Outline each blood parasite and name the species.
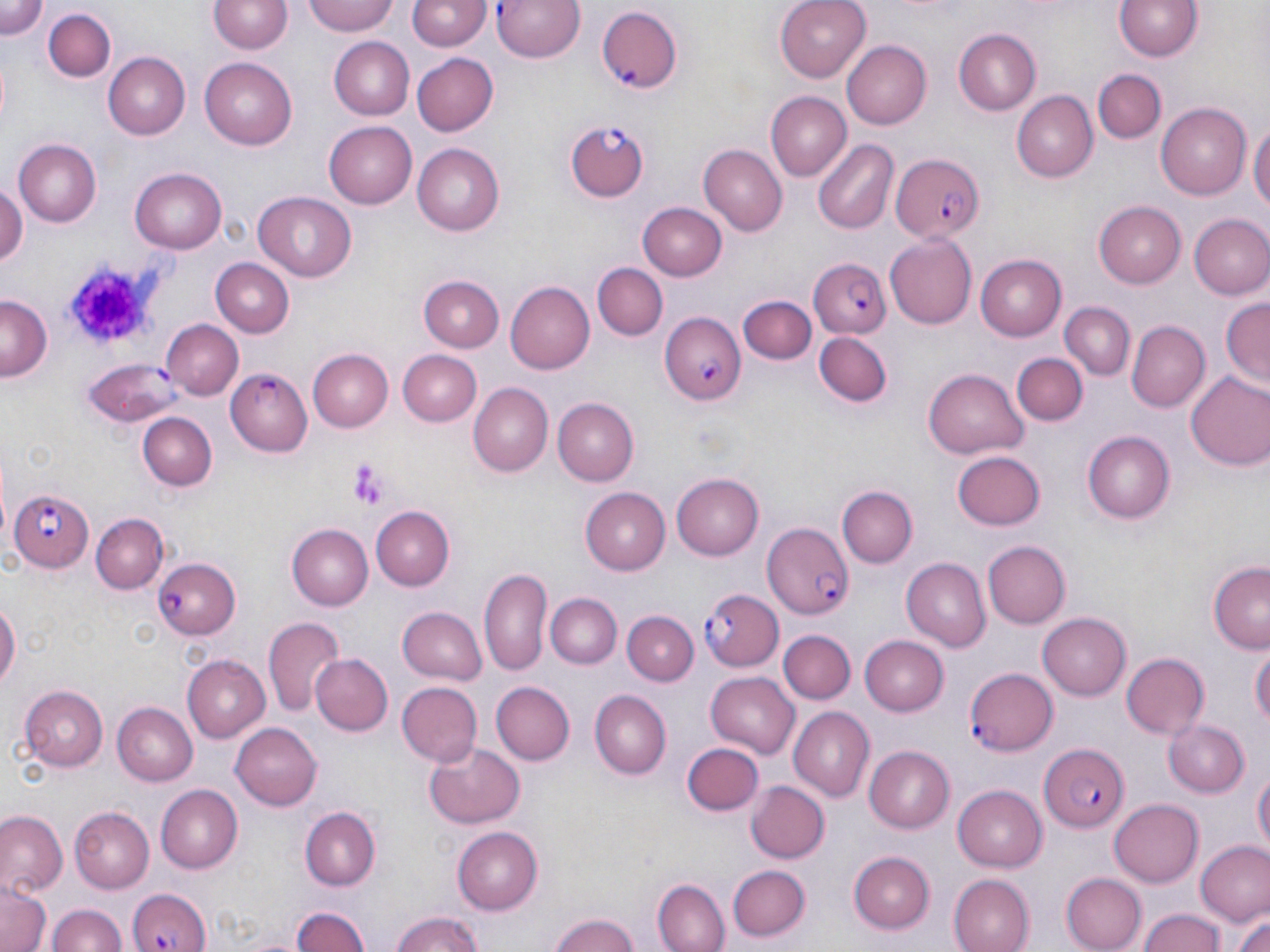

Approximate bounding boxes as named x1/y1/x2/y2 corners in pixels.
Plasmodium falciparum-infected red blood cells: (x1=494, y1=0, x2=587, y2=65), (x1=596, y1=6, x2=684, y2=91), (x1=566, y1=122, x2=650, y2=199), (x1=892, y1=154, x2=985, y2=243), (x1=807, y1=257, x2=892, y2=339), (x1=660, y1=311, x2=744, y2=406), (x1=83, y1=360, x2=183, y2=425), (x1=224, y1=369, x2=313, y2=457), (x1=11, y1=489, x2=92, y2=573), (x1=760, y1=522, x2=853, y2=618), (x1=155, y1=557, x2=240, y2=639), (x1=700, y1=589, x2=782, y2=670), (x1=964, y1=666, x2=1057, y2=756), (x1=1037, y1=742, x2=1130, y2=832), (x1=127, y1=886, x2=210, y2=952).
No Plasmodium ovale, Plasmodium malariae, Plasmodium vivax, Babesia divergens, or Trypanosoma brucei observed.

Platelet locations: (x1=65, y1=258, x2=160, y2=350), (x1=348, y1=461, x2=390, y2=510). Uninfected red blood cell locations: (x1=0, y1=0, x2=49, y2=39), (x1=302, y1=0, x2=399, y2=37), (x1=773, y1=0, x2=871, y2=83), (x1=1113, y1=0, x2=1206, y2=62), (x1=209, y1=1, x2=291, y2=55), (x1=408, y1=1, x2=488, y2=51), (x1=42, y1=7, x2=116, y2=80), (x1=951, y1=28, x2=1041, y2=115), (x1=328, y1=36, x2=414, y2=118), (x1=840, y1=38, x2=930, y2=130), (x1=410, y1=52, x2=496, y2=137), (x1=104, y1=53, x2=190, y2=138), (x1=200, y1=58, x2=297, y2=147), (x1=1094, y1=70, x2=1164, y2=143), (x1=1010, y1=90, x2=1098, y2=181), (x1=764, y1=91, x2=850, y2=180), (x1=1156, y1=104, x2=1252, y2=198), (x1=1250, y1=119, x2=1269, y2=224), (x1=325, y1=123, x2=416, y2=207), (x1=813, y1=139, x2=898, y2=234), (x1=13, y1=140, x2=102, y2=227), (x1=412, y1=144, x2=505, y2=235), (x1=698, y1=146, x2=787, y2=234), (x1=131, y1=168, x2=227, y2=253), (x1=0, y1=183, x2=25, y2=273), (x1=254, y1=193, x2=357, y2=281), (x1=1093, y1=201, x2=1187, y2=287), (x1=639, y1=203, x2=726, y2=280), (x1=1189, y1=214, x2=1270, y2=299), (x1=885, y1=234, x2=976, y2=329), (x1=975, y1=255, x2=1066, y2=340), (x1=210, y1=258, x2=293, y2=336), (x1=592, y1=263, x2=667, y2=341), (x1=420, y1=273, x2=504, y2=352), (x1=503, y1=281, x2=594, y2=375), (x1=0, y1=296, x2=50, y2=380), (x1=738, y1=296, x2=815, y2=364), (x1=1221, y1=299, x2=1269, y2=391), (x1=1061, y1=302, x2=1133, y2=380), (x1=1126, y1=319, x2=1209, y2=411), (x1=160, y1=320, x2=241, y2=401), (x1=816, y1=330, x2=894, y2=408), (x1=309, y1=350, x2=395, y2=433), (x1=397, y1=351, x2=481, y2=425), (x1=1014, y1=354, x2=1085, y2=426), (x1=923, y1=369, x2=1029, y2=459), (x1=1185, y1=371, x2=1270, y2=472), (x1=470, y1=383, x2=552, y2=476), (x1=551, y1=398, x2=638, y2=486), (x1=139, y1=412, x2=215, y2=490), (x1=1083, y1=432, x2=1176, y2=524), (x1=952, y1=451, x2=1045, y2=530), (x1=672, y1=474, x2=765, y2=559), (x1=839, y1=486, x2=918, y2=568), (x1=580, y1=488, x2=670, y2=573), (x1=369, y1=506, x2=453, y2=590), (x1=91, y1=512, x2=167, y2=592), (x1=287, y1=524, x2=373, y2=609), (x1=981, y1=541, x2=1069, y2=629), (x1=900, y1=558, x2=991, y2=650), (x1=1208, y1=562, x2=1270, y2=653), (x1=479, y1=567, x2=550, y2=674), (x1=547, y1=592, x2=620, y2=668), (x1=0, y1=598, x2=18, y2=695), (x1=397, y1=604, x2=487, y2=684), (x1=623, y1=610, x2=699, y2=683), (x1=1038, y1=612, x2=1131, y2=700), (x1=264, y1=617, x2=346, y2=714), (x1=778, y1=630, x2=855, y2=705), (x1=857, y1=635, x2=948, y2=716), (x1=1251, y1=640, x2=1269, y2=729), (x1=1120, y1=652, x2=1210, y2=741), (x1=182, y1=654, x2=271, y2=740), (x1=311, y1=654, x2=393, y2=736), (x1=706, y1=671, x2=800, y2=756), (x1=490, y1=681, x2=573, y2=767), (x1=15, y1=682, x2=108, y2=775), (x1=395, y1=682, x2=482, y2=768), (x1=589, y1=690, x2=671, y2=779), (x1=112, y1=703, x2=197, y2=786), (x1=788, y1=708, x2=874, y2=801), (x1=1164, y1=718, x2=1250, y2=796), (x1=230, y1=723, x2=322, y2=810), (x1=423, y1=739, x2=527, y2=828), (x1=682, y1=742, x2=763, y2=816), (x1=865, y1=746, x2=954, y2=832), (x1=1252, y1=765, x2=1269, y2=855), (x1=745, y1=781, x2=829, y2=865), (x1=156, y1=785, x2=243, y2=871), (x1=952, y1=785, x2=1048, y2=871), (x1=1108, y1=800, x2=1203, y2=887), (x1=301, y1=806, x2=380, y2=889), (x1=72, y1=807, x2=155, y2=893), (x1=0, y1=812, x2=65, y2=895), (x1=453, y1=825, x2=543, y2=912), (x1=1196, y1=842, x2=1269, y2=927), (x1=849, y1=852, x2=935, y2=934), (x1=727, y1=865, x2=810, y2=942), (x1=1061, y1=871, x2=1147, y2=951), (x1=948, y1=875, x2=1034, y2=952), (x1=653, y1=880, x2=729, y2=952), (x1=0, y1=884, x2=50, y2=952), (x1=47, y1=903, x2=123, y2=952), (x1=289, y1=906, x2=373, y2=952), (x1=1228, y1=908, x2=1270, y2=952), (x1=1136, y1=909, x2=1229, y2=952), (x1=388, y1=911, x2=488, y2=952), (x1=548, y1=913, x2=645, y2=952). Slide-level diagnosis: Plasmodium falciparum. Optical microscopy. May-Grünwald-Giemsa stain. Image is 1270×952 pixels. Thin blood smear. Captured at 1000x magnification. One field of a larger specimen.